Classify this cell by malaria status.
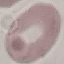

It is uninfected.

Photographed with a smartphone camera at the microscope eyepiece. Giemsa-stained preparation. Thin blood smear. Cell patch, automatically extracted from a larger field of view and resized to 64 × 64 pixels.